Assess the morphology of the erythrocytes.
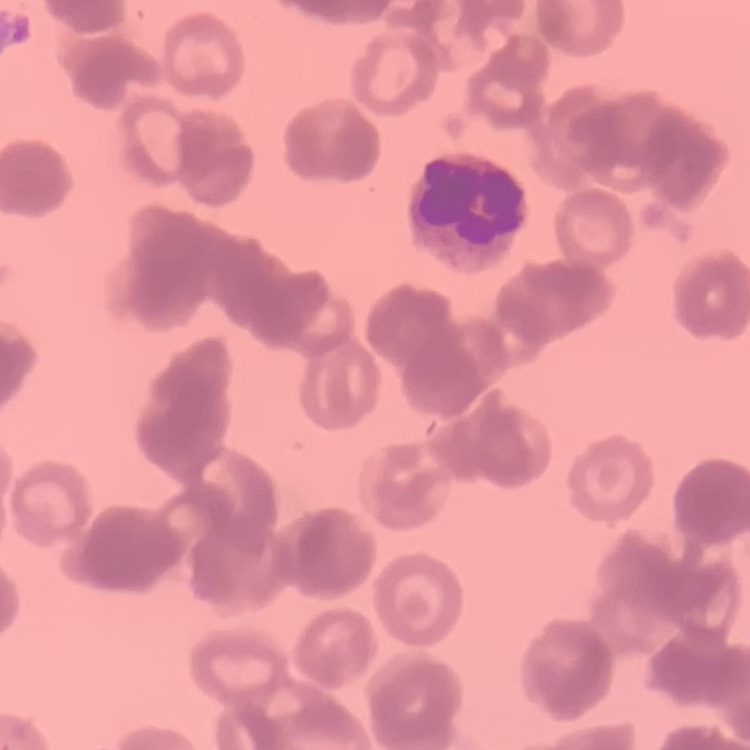
Rouleaux formation.

Field's or Giemsa stain. Square crop of a larger photomicrograph. Thin blood film.